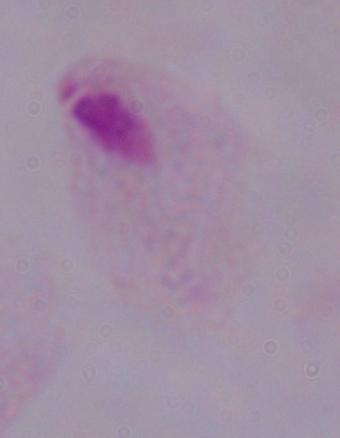 A trichomonad is shown. Captured at 1000x magnification. Micrograph.